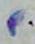
1000x magnification. Toxoplasma gondii is shown. Micrograph.